Identify the parasite.
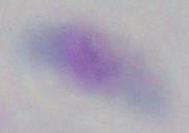
Toxoplasma gondii.

Summary:
  - Modality: micrograph
  - Magnification: 1000x